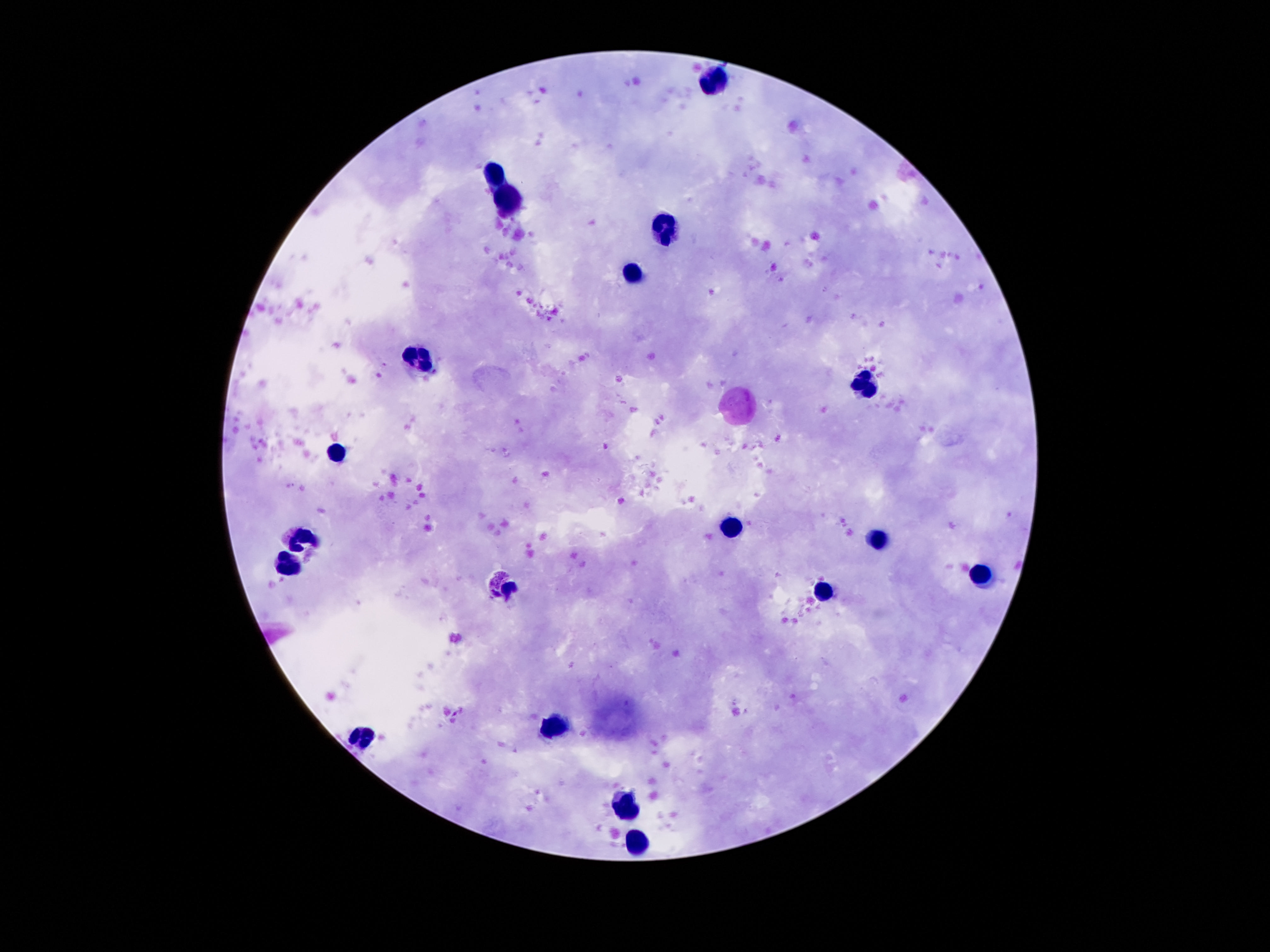 Approximate centers as {x, y} in pixels. Leukocyte locations: {716, 80}, {496, 176}, {507, 206}, {664, 225}, {634, 273}, {423, 358}, {867, 389}, {335, 451}, {735, 525}, {307, 538}, {880, 538}, {287, 566}, {979, 572}, {559, 726}, {363, 738}, {626, 807}, {636, 841}. Thick blood smear. Giemsa-stained preparation. Single field of view. Photographed through the microscope eyepiece with a smartphone camera. 100x magnification. Patient malaria status: uninfected. Image is 1270×952 pixels.